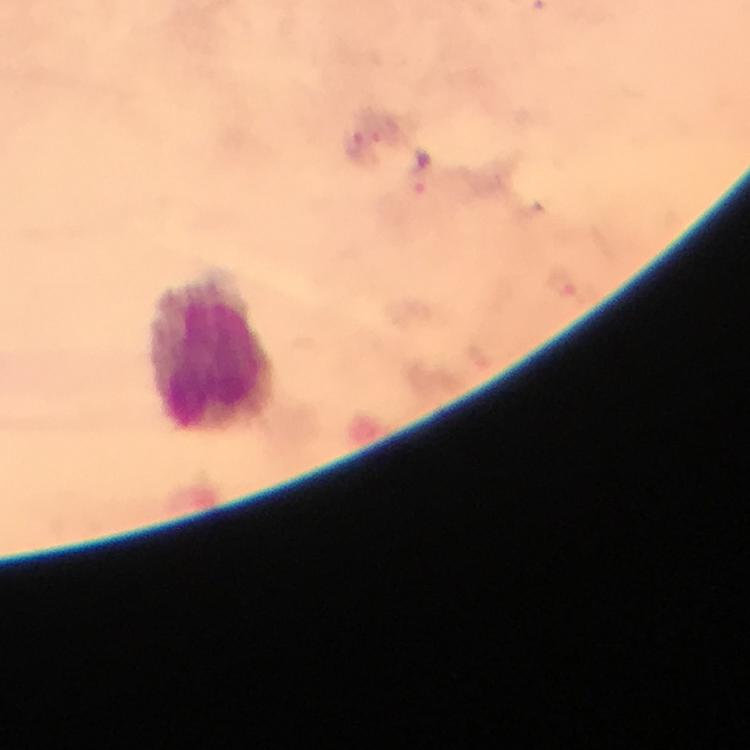

capture = smartphone mounted on the microscope
stain = Giemsa
image size = 750×750 pixels
preparation = thick blood film
immersion oil = applied
magnification = 100x
context = from a diagnostic examination for malaria
Plasmodium parasites = none seen
cropped from = one field of view
leukocyte locations = approximate centers as {x, y} in pixels: {215, 355}